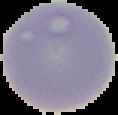
{
  "result": "no malaria parasites seen",
  "image_size": "118×115 pixels",
  "image_type": "segmented cell region with the area outside set to black",
  "preparation": "thin blood film"
}